Point out each malaria parasite.
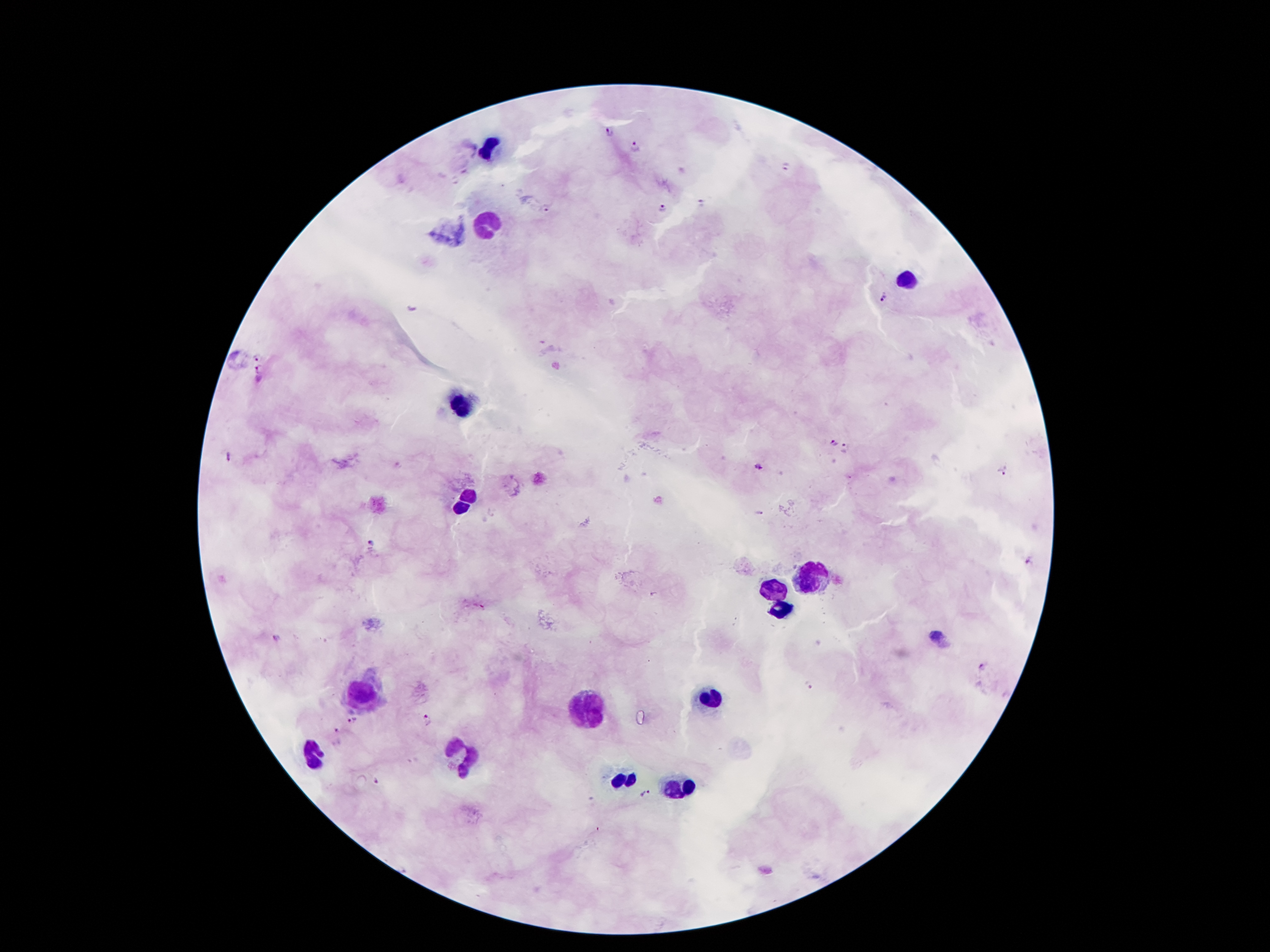

Approximate object centers, in pixels from the top-left corner.
Malaria parasites: (x=611, y=132), (x=635, y=147), (x=787, y=166), (x=700, y=204), (x=546, y=207), (x=663, y=209), (x=885, y=299), (x=257, y=356), (x=260, y=370), (x=832, y=443), (x=845, y=446), (x=229, y=456), (x=757, y=466), (x=1004, y=469), (x=370, y=541), (x=1031, y=563), (x=935, y=633), (x=276, y=639), (x=981, y=668), (x=810, y=687), (x=353, y=720), (x=428, y=722), (x=336, y=730), (x=377, y=779), (x=646, y=794).

Leukocyte locations: (x=489, y=146), (x=489, y=227), (x=907, y=280), (x=459, y=404), (x=466, y=501), (x=805, y=577), (x=776, y=590), (x=781, y=610), (x=364, y=696), (x=710, y=700), (x=586, y=711), (x=316, y=751), (x=464, y=756), (x=626, y=780), (x=681, y=789). 100x magnification. Smartphone photograph taken through the microscope eyepiece. Patient malaria status: infected with Plasmodium falciparum. Single field of view. Giemsa-stained preparation. Thick peripheral-blood smear. Image is 1270×952 pixels.